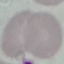

{
  "malaria_status": "uninfected",
  "preparation": "thin blood smear",
  "stain": "Giemsa",
  "image_type": "automatically extracted cell patch, resized to 64 × 64 pixels",
  "capture": "smartphone through the microscope eyepiece"
}